Outline each uninfected red blood cell.
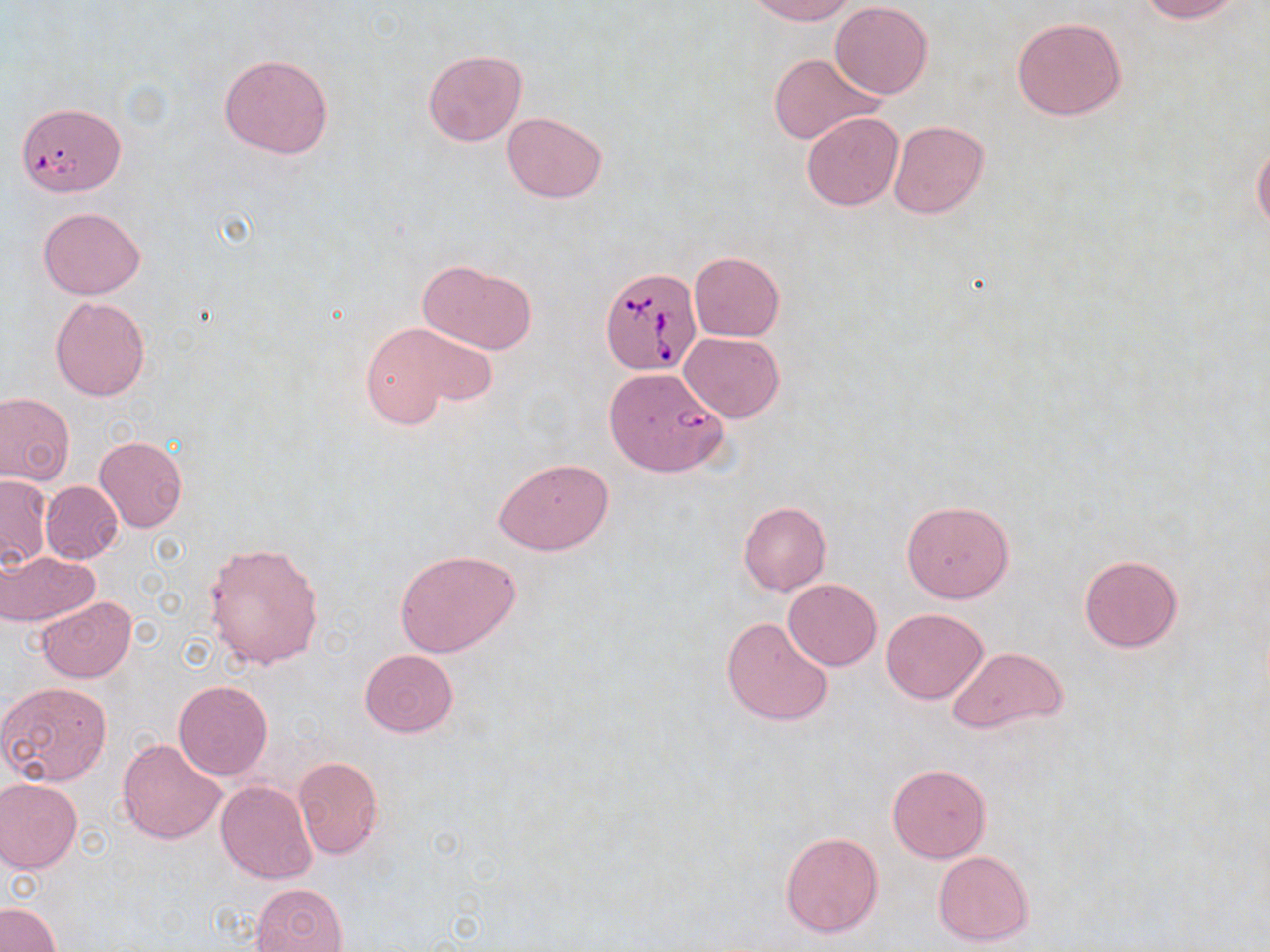
Approximate bounding boxes as (x1,y1)-(x2,y2) corner pairs in pixels.
Uninfected red blood cells: (745,0)-(859,24), (1138,0)-(1246,22), (831,2)-(934,99), (1011,16)-(1126,121), (422,48)-(528,148), (768,52)-(883,146), (218,53)-(333,159), (801,111)-(905,212), (502,112)-(608,202), (888,120)-(991,219), (1252,137)-(1270,235), (38,206)-(145,298), (689,251)-(784,341), (419,260)-(538,354), (50,296)-(152,401), (358,326)-(475,429), (680,332)-(784,423), (602,367)-(727,478), (0,393)-(75,485), (94,435)-(187,533), (494,459)-(614,555), (1,474)-(52,568), (41,480)-(123,564), (900,499)-(1015,603), (737,500)-(831,596), (203,542)-(325,671), (1,550)-(99,626), (395,550)-(521,657), (1078,554)-(1184,652), (783,579)-(882,670), (36,596)-(138,683), (880,607)-(988,704), (721,615)-(835,726), (946,645)-(1069,736), (359,649)-(458,737), (173,680)-(274,780), (0,682)-(113,787), (117,738)-(227,844), (292,755)-(383,860), (887,763)-(991,862), (0,778)-(83,872), (215,780)-(316,883), (781,831)-(883,938), (932,851)-(1035,947), (249,883)-(347,952), (0,903)-(61,952).

Summary:
  - Babesia divergens-infected red blood cell locations: (20,105)-(131,197), (599,264)-(703,374)
  - Slide-level diagnosis: Babesia divergens
  - Preparation: thin blood smear
  - Field of view: single
  - Modality: light microscopy
  - Stain: May-Grünwald-Giemsa
  - Image size: 1270×952 pixels
  - Magnification: 1000x